Give the position of every Plasmodium parasite.
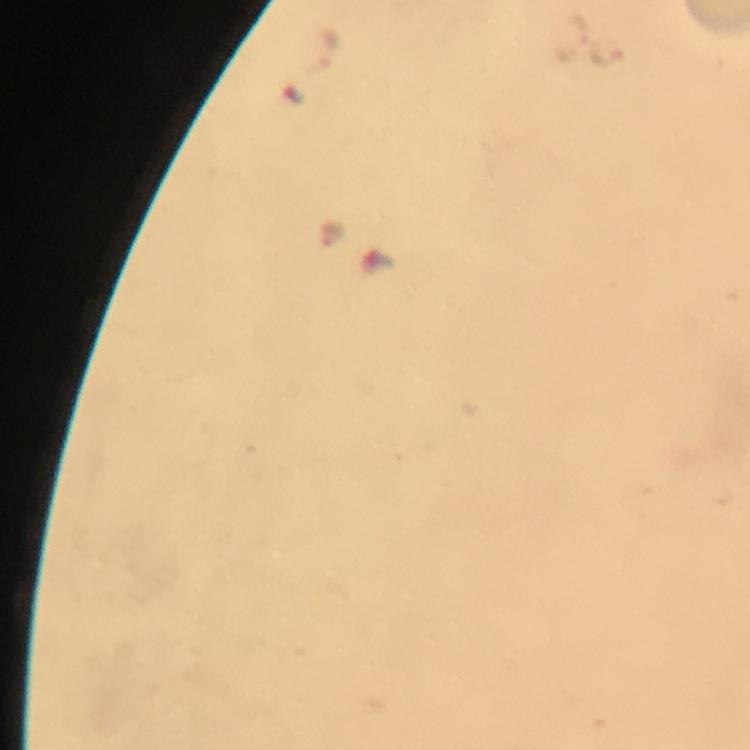

Approximate centers as [x, y] in pixels.
Plasmodium parasites: [570, 37], [322, 50], [605, 51], [329, 234].

Summary:
  - Magnification: 100x
  - Preparation: thick smear
  - Image size: 750×750 pixels
  - Stain: Giemsa
  - Immersion oil: applied
  - Cropped from: one field of view
  - Capture: smartphone photograph through a microscope
  - Context: from a malaria diagnostic workup